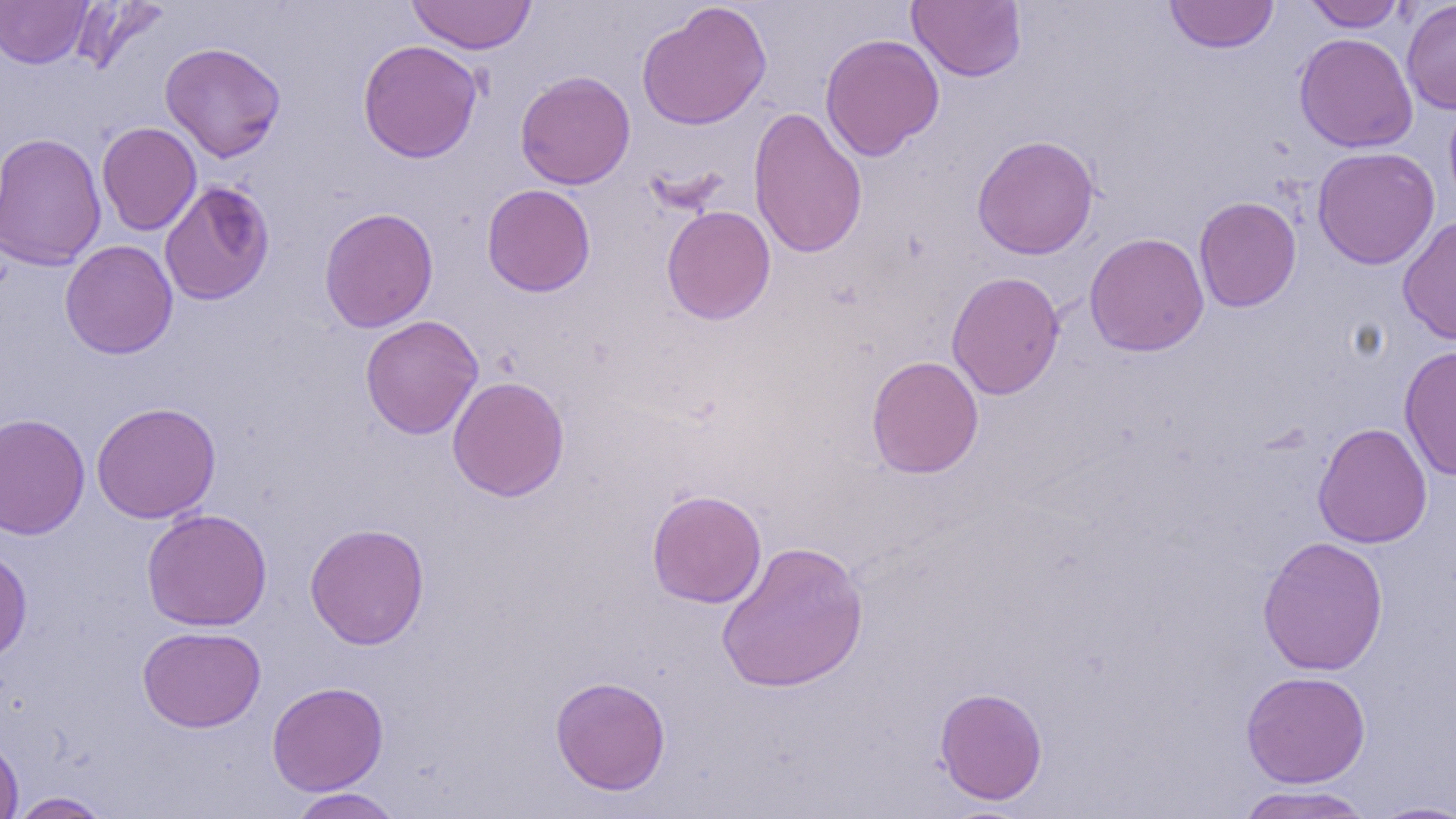
Approximate bounding boxes as (x1,y1)-(x2,y2) corner pairs in pixels. Uninfected red blood cell locations: (69,0)-(170,76), (406,0)-(537,54), (906,0)-(1026,82), (1401,0)-(1456,114), (0,1)-(93,68), (1164,1)-(1278,53), (1304,1)-(1406,31), (636,2)-(772,130), (1294,32)-(1418,153), (819,33)-(945,161), (357,39)-(482,163), (159,42)-(286,162), (515,70)-(635,189), (1444,94)-(1456,217), (748,107)-(868,259), (96,121)-(201,235), (1,132)-(107,271), (972,134)-(1099,260), (1312,146)-(1440,270), (159,180)-(275,305), (482,183)-(596,297), (1194,196)-(1302,313), (661,205)-(776,325), (319,207)-(438,333), (1397,214)-(1456,346), (1084,232)-(1210,356), (60,240)-(178,359), (946,271)-(1065,400), (360,315)-(483,439), (1398,344)-(1456,482), (866,355)-(984,479), (447,376)-(569,502), (91,401)-(221,524), (0,414)-(90,539), (1313,422)-(1433,548), (646,489)-(767,608), (141,508)-(273,631), (304,522)-(430,650), (1257,535)-(1389,676), (716,540)-(869,694), (0,546)-(32,664), (137,625)-(266,732), (1241,670)-(1371,788), (550,676)-(671,795), (266,681)-(388,795), (934,686)-(1048,805), (0,731)-(23,818), (1234,784)-(1377,819), (288,788)-(404,818), (8,791)-(114,818), (1366,800)-(1456,818). Slide-level diagnosis: no evidence of blood parasites. Image is 1456×819 pixels. Captured at 1000x magnification. Thin blood smear. One field of a larger specimen. Optical microscopy.